Comment on the morphology of the red blood cells.
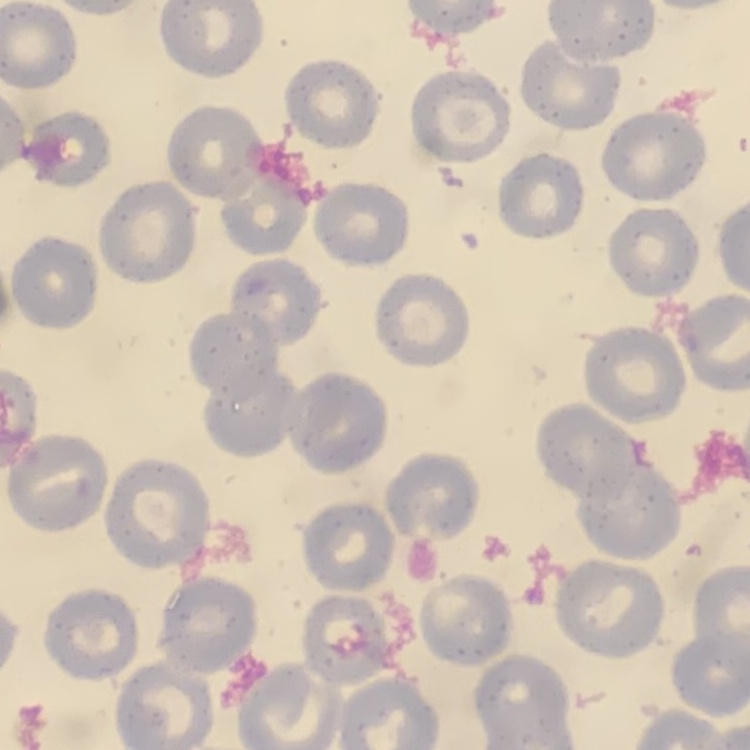

No rouleaux formation.

Summary:
  - Stain: Field's or Giemsa
  - Preparation: thin blood smear
  - Image type: square crop of a larger photomicrograph